Report the malaria status of this cell.
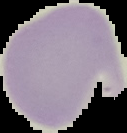
It is uninfected.

preparation = thin blood film
image type = segmented cell region on a black background
image size = 127×133 pixels